Assess this cell for malaria.
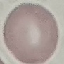
It is uninfected.

Summary:
  - Image type: automatically extracted cell patch, resized to 64 × 64 pixels
  - Capture: smartphone through the microscope eyepiece
  - Stain: Giemsa
  - Preparation: thin blood smear